State which parasite is depicted.
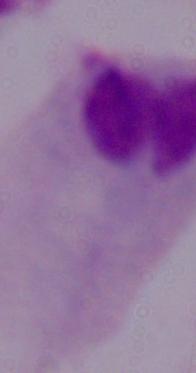
A trichomonad.

Summary:
  - Magnification: 1000x
  - Modality: micrograph